Describe the morphology of the erythrocytes.
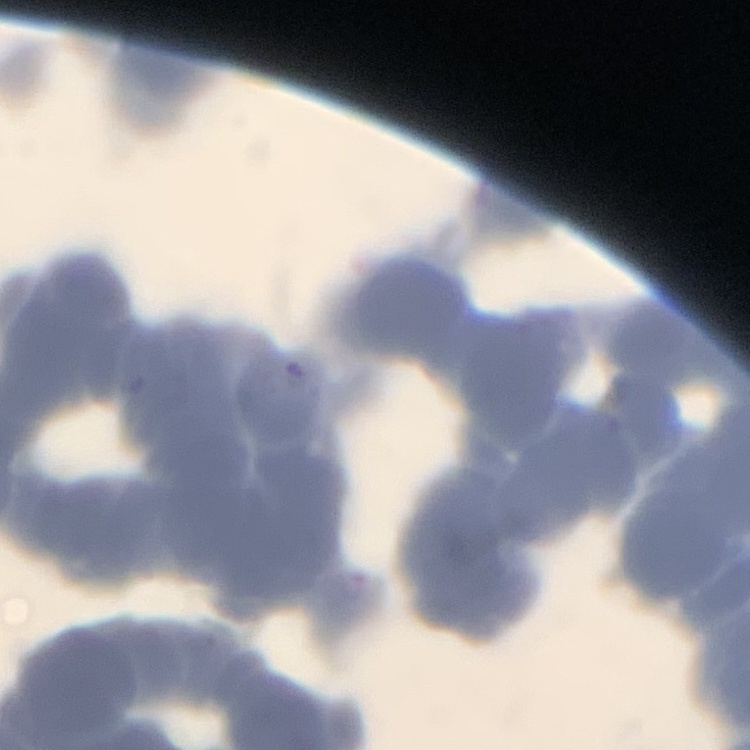
They show rouleaux formation.

Summary:
  - Image type: square crop of a larger photomicrograph
  - Stain: Field's or Giemsa
  - Preparation: thin peripheral smear